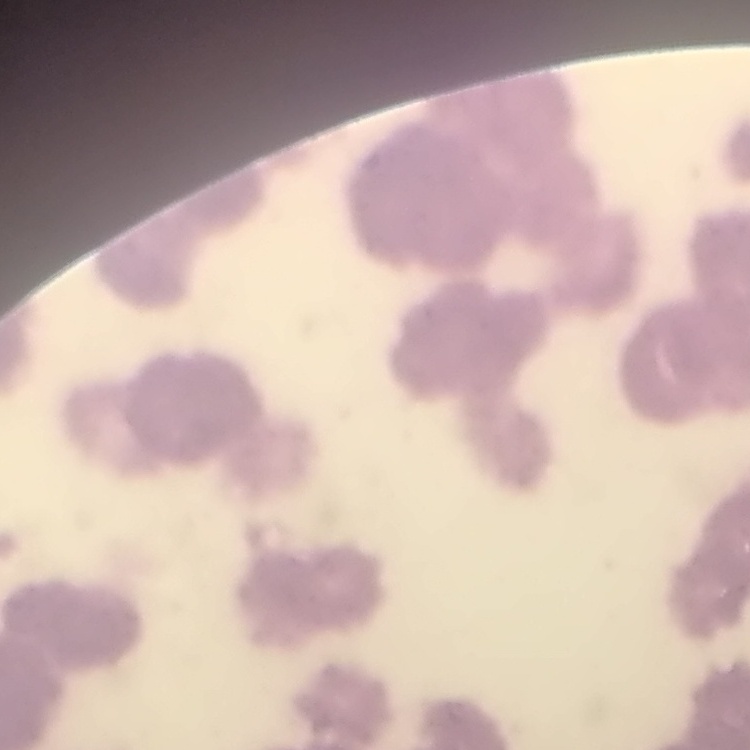

Summary:
  - Erythrocyte morphology: rouleaux formation
  - Stain: Field's or Giemsa
  - Image type: square crop of a larger photomicrograph
  - Preparation: thin peripheral smear